Classify this cell by malaria status.
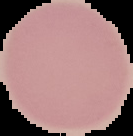
It is uninfected.

Cell region segmented out of the field of view; the surrounding area is masked to black. From a thin blood film. Image is 133×136 pixels.